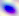
Summary:
  - Identification: Toxoplasma gondii
  - Magnification: 400x
  - Modality: photomicrograph